Classify this cell by malaria status.
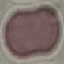

It is uninfected.

Summary:
  - Preparation: thin blood smear
  - Capture: smartphone camera at the microscope eyepiece
  - Stain: Giemsa
  - Image type: cell patch, automatically extracted from a larger field of view and resized to 64 × 64 pixels